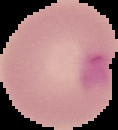

Malaria status: parasitized. The area outside the segmented cell region is set to black. Image is 118×130 pixels. From a thin blood smear.